Locate every malaria parasite.
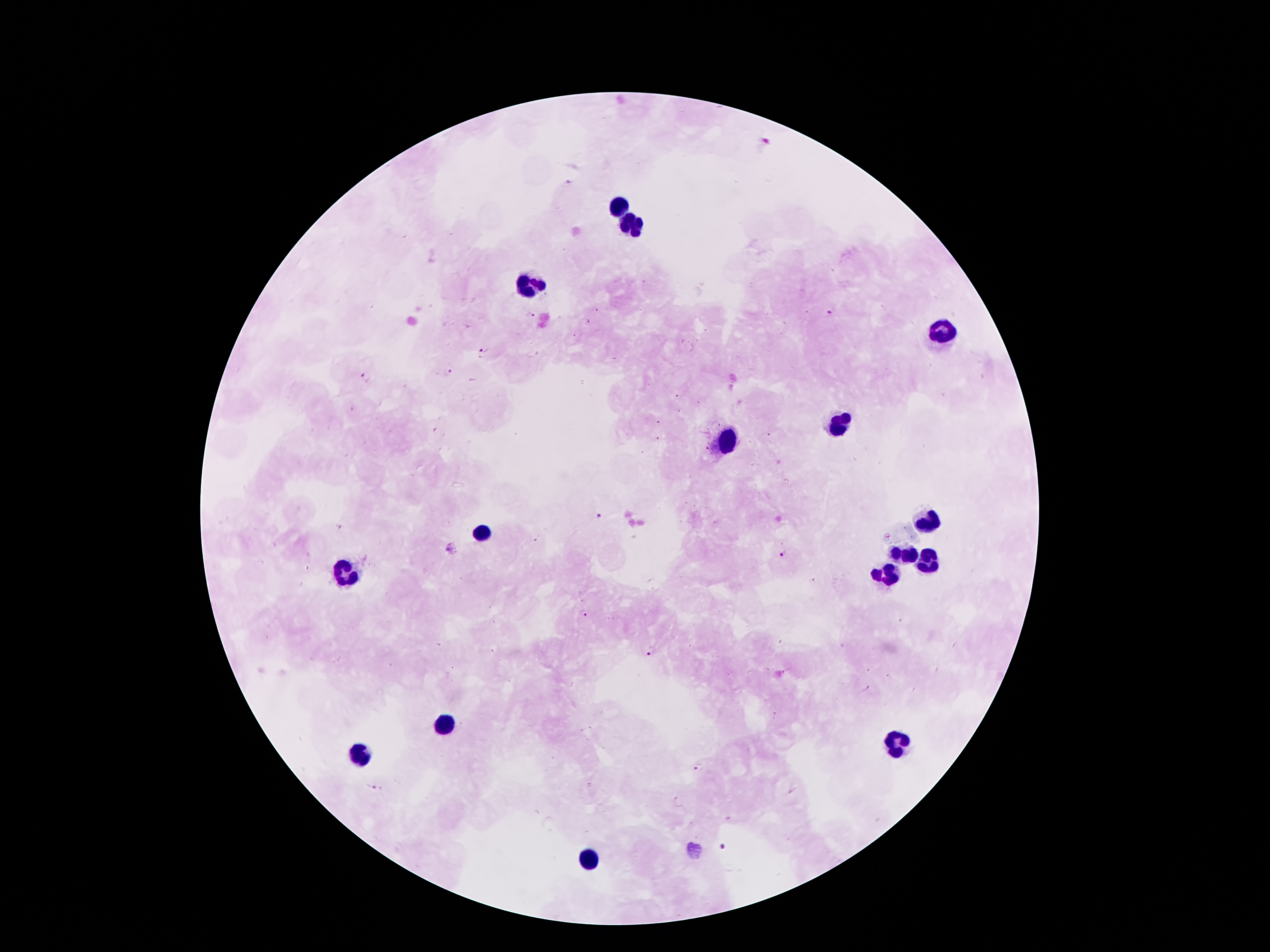
Approximate centers as (x, y) in pixels.
Malaria parasites: (597, 309), (528, 313), (829, 314), (588, 322), (575, 335), (682, 342), (483, 351), (448, 372), (365, 377), (677, 395), (698, 402), (679, 411), (436, 430), (767, 436), (599, 515), (339, 527), (451, 548), (784, 555), (813, 580), (583, 613), (651, 652), (866, 690), (697, 767), (370, 787), (722, 849).

Leukocyte locations: (622, 203), (628, 224), (528, 285), (942, 332), (839, 426), (727, 439), (928, 525), (479, 533), (903, 554), (926, 560), (885, 574), (342, 576), (444, 724), (893, 742), (358, 755), (587, 857). Thick peripheral-blood smear. Giemsa-stained preparation. Patient malaria status: infected with Plasmodium falciparum. Image is 1270×952 pixels. 100x magnification. Single field of view. Photographed through the microscope eyepiece with a smartphone camera.